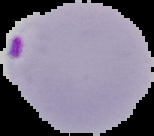

Summary:
  - Preparation: thin blood smear
  - Malaria status: parasitized
  - Image type: segmented cell region with the area outside set to black
  - Image size: 154×136 pixels